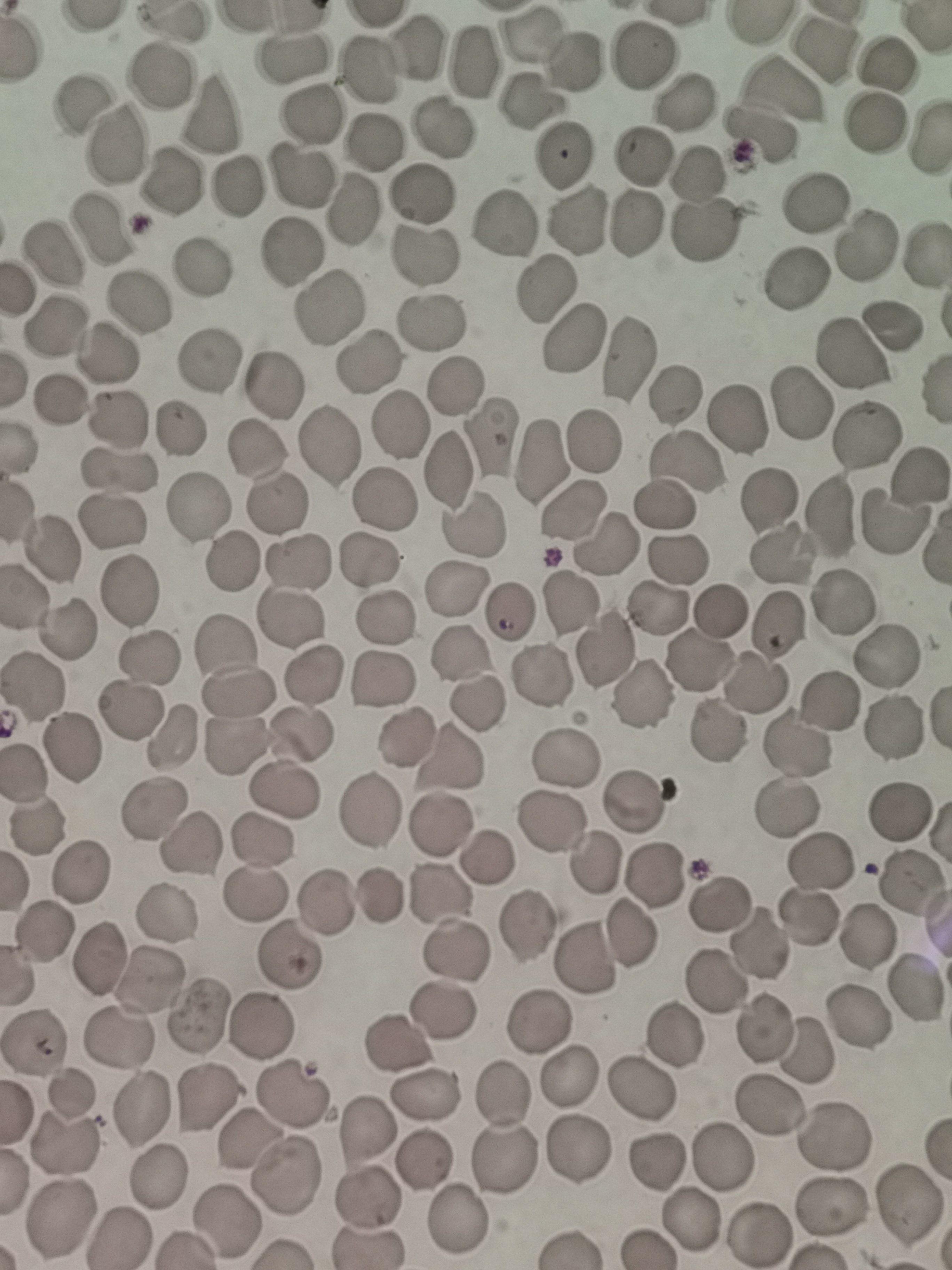

{
  "cell_locations": "approximate centers as [x, y] in pixels: [530, 35], [418, 47], [825, 50], [642, 55], [293, 56], [572, 58], [475, 63], [370, 70], [157, 78], [781, 88], [530, 101], [682, 103], [78, 108], [212, 112], [314, 117], [872, 127], [439, 130], [758, 137], [373, 143], [114, 147], [563, 156], [639, 157], [695, 170], [297, 174], [170, 186], [236, 189], [419, 194], [815, 204], [350, 211], [576, 221], [635, 224], [500, 226], [99, 228], [702, 233], [291, 251], [50, 254], [422, 256], [200, 269], [795, 280], [544, 289], [136, 304], [327, 304], [434, 323], [891, 325], [55, 327], [572, 341], [109, 354], [855, 355], [626, 357], [209, 360], [367, 361], [273, 384], [453, 385], [675, 395], [57, 401], [801, 403], [116, 418], [739, 419], [400, 425], [176, 429], [865, 435], [489, 438], [592, 441], [328, 443], [256, 452], [541, 461], [687, 464], [120, 470], [448, 471], [916, 477], [381, 498], [769, 502], [277, 506], [665, 506], [197, 508], [572, 512], [830, 515], [108, 519], [894, 522], [471, 529], [608, 548], [53, 550], [783, 554], [677, 558], [368, 560], [299, 562], [231, 564], [129, 592], [456, 592], [842, 601], [566, 604], [658, 608], [722, 610], [508, 612], [385, 616], [291, 619], [777, 626], [69, 629], [606, 650], [461, 653], [891, 656], [148, 658], [701, 661], [313, 676], [540, 676], [382, 681], [755, 683], [33, 686], [237, 694], [643, 694], [826, 704], [477, 706], [131, 710], [892, 730], [717, 732], [304, 734], [402, 738], [172, 739], [796, 743], [75, 749], [563, 757], [450, 759], [24, 773], [285, 792], [634, 801], [156, 809], [368, 809], [787, 810], [897, 813], [441, 822], [548, 822], [38, 827], [261, 842], [190, 847], [489, 856], [820, 859], [595, 865], [78, 876], [657, 877], [911, 884], [256, 893], [381, 893], [443, 895], [327, 901], [717, 906], [166, 913], [809, 918], [523, 925], [44, 933], [629, 936], [863, 937], [761, 946], [457, 947], [96, 958], [288, 958], [587, 958], [150, 982], [715, 983], [918, 989], [444, 1012], [198, 1017], [857, 1019], [537, 1023], [260, 1024], [764, 1028], [676, 1034], [33, 1039], [119, 1040], [395, 1047], [810, 1055], [567, 1079], [643, 1090], [426, 1094], [505, 1094], [293, 1095], [72, 1097], [208, 1100], [140, 1109], [768, 1109], [365, 1133], [834, 1136], [249, 1143], [67, 1148], [578, 1150], [724, 1158], [506, 1160], [425, 1161], [658, 1161], [288, 1178], [157, 1179], [370, 1202], [909, 1203], [831, 1206], [226, 1219], [459, 1219], [60, 1220], [690, 1223], [758, 1234], [119, 1238]",
  "field_of_view": "single",
  "capture": "smartphone through the microscope eyepiece",
  "image_size": "952×1270 pixels",
  "preparation": "thin smear",
  "stain": "Giemsa"
}